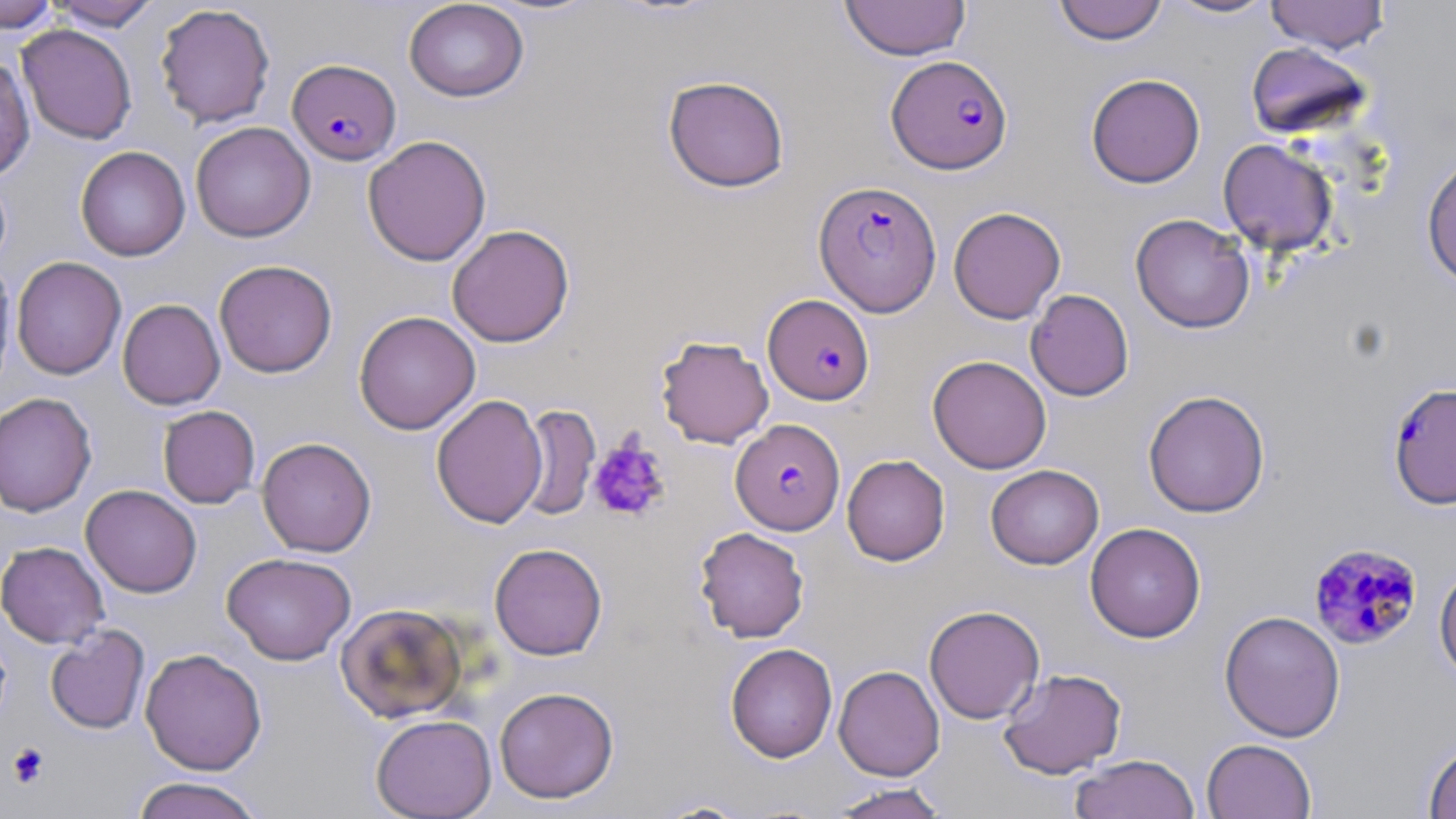
slide-level diagnosis = Plasmodium falciparum
image size = 1456×819 pixels
preparation = thin blood film
modality = optical microscopy
stain = May-Grünwald-Giemsa
magnification = 1000x
Plasmodium falciparum-infected red blood cell locations = approximate bounding boxes as (x1, y1, x2, y2) in pixels: (887, 54, 1013, 174), (287, 59, 402, 166), (814, 181, 942, 316), (763, 294, 874, 404), (1386, 381, 1456, 510), (731, 418, 845, 535), (1308, 543, 1423, 650)
uninfected red blood cell locations = approximate bounding boxes as (x1, y1, x2, y2) in pixels: (403, 0, 529, 102), (840, 0, 972, 61), (1052, 0, 1167, 45), (1165, 0, 1278, 19), (1265, 0, 1390, 53), (0, 1, 59, 31), (48, 1, 162, 31), (154, 3, 275, 129), (17, 24, 137, 144), (1245, 41, 1374, 140), (0, 55, 35, 180), (1085, 73, 1205, 188), (662, 75, 790, 193), (190, 121, 316, 242), (362, 135, 492, 266), (1217, 139, 1339, 256), (75, 146, 191, 261), (1421, 152, 1456, 290), (948, 206, 1066, 324), (1130, 214, 1255, 333), (447, 224, 575, 347), (11, 256, 126, 380), (0, 257, 16, 394), (214, 260, 337, 378), (1025, 289, 1134, 401), (117, 299, 225, 410), (354, 310, 481, 435), (655, 335, 774, 448), (927, 355, 1052, 474), (1143, 390, 1271, 518), (0, 392, 97, 517), (431, 394, 548, 528), (518, 404, 600, 521), (158, 405, 260, 508), (257, 437, 376, 557), (842, 454, 950, 566), (986, 464, 1104, 569), (80, 484, 202, 598), (1085, 522, 1206, 642), (694, 527, 809, 643), (0, 541, 109, 648), (489, 543, 608, 660), (222, 552, 356, 665), (1434, 561, 1456, 687), (335, 602, 468, 723), (924, 605, 1045, 724), (1219, 609, 1345, 742), (45, 625, 149, 734), (725, 643, 837, 763), (140, 648, 267, 775), (833, 665, 945, 781), (997, 668, 1127, 779), (494, 686, 619, 803), (370, 714, 497, 819), (1201, 738, 1317, 819), (1422, 739, 1456, 819), (1069, 753, 1201, 818), (130, 776, 267, 819), (826, 783, 952, 818), (650, 798, 753, 818)
field of view = single
platelet locations = approximate bounding boxes as (x1, y1, x2, y2) in pixels: (588, 438, 671, 523), (7, 742, 50, 788)